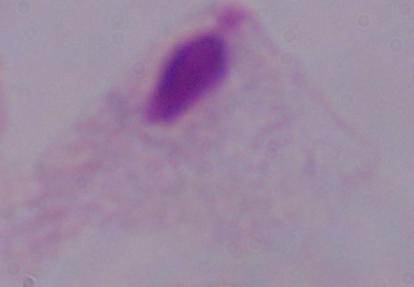

{
  "identification": "trichomonad",
  "modality": "photomicrograph",
  "magnification": "1000x"
}